Assess this cell for malaria.
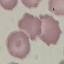

Uninfected.

stain = Giemsa
preparation = thin blood smear
capture = smartphone through the microscope eyepiece
image type = cell patch, automatically extracted from a larger field of view and resized to 64 × 64 pixels